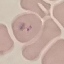
Malaria status: uninfected. Giemsa stain. Photographed with a smartphone camera at the microscope eyepiece. Cell patch, automatically extracted from a larger field of view and resized to 64 × 64 pixels. Thin blood film.